Classify this cell by malaria status.
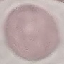

It is uninfected.

preparation = thin blood smear
stain = Giemsa
image type = automatically extracted cell patch, resized to 64 × 64 pixels
capture = smartphone through the microscope eyepiece